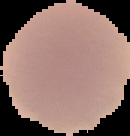
result: no Plasmodium parasites detected
image_size: 130×136 pixels
image_type: segmented cell region on a black background
preparation: thin blood smear